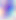
Summary:
  - Magnification: 400x
  - Modality: micrograph
  - Identification: Toxoplasma gondii